Evaluate for Plasmodium parasites.
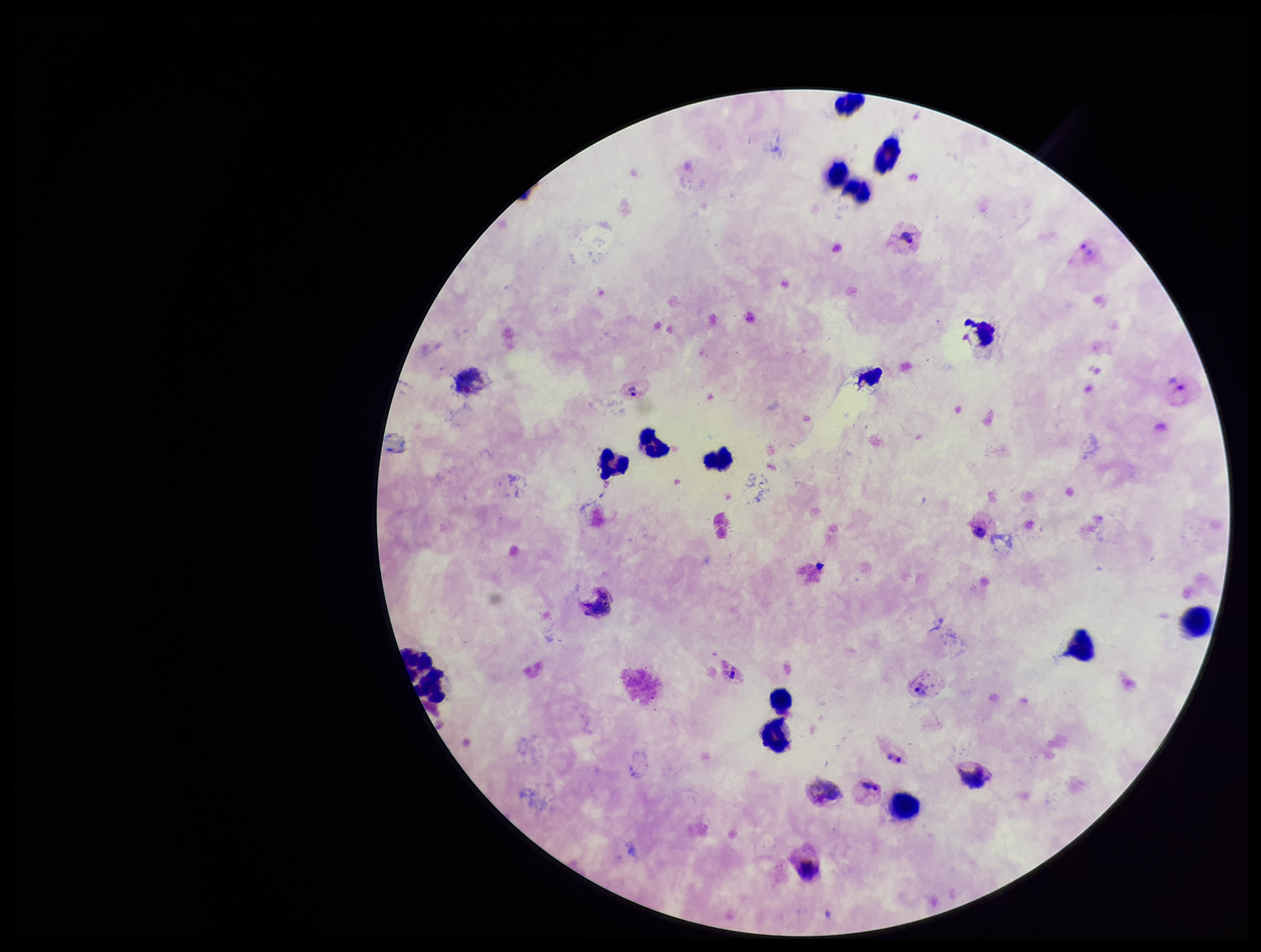
Identified.

Summary:
  - Patient malaria status: infected
  - Capture: smartphone photograph through the microscope eyepiece
  - Leukocyte count: 13
  - Field of view: single
  - Image size: 1261×952 pixels
  - Preparation: thick blood smear
  - Stain: Giemsa
  - Parasite count: 7
  - Species reported for this patient: Plasmodium vivax